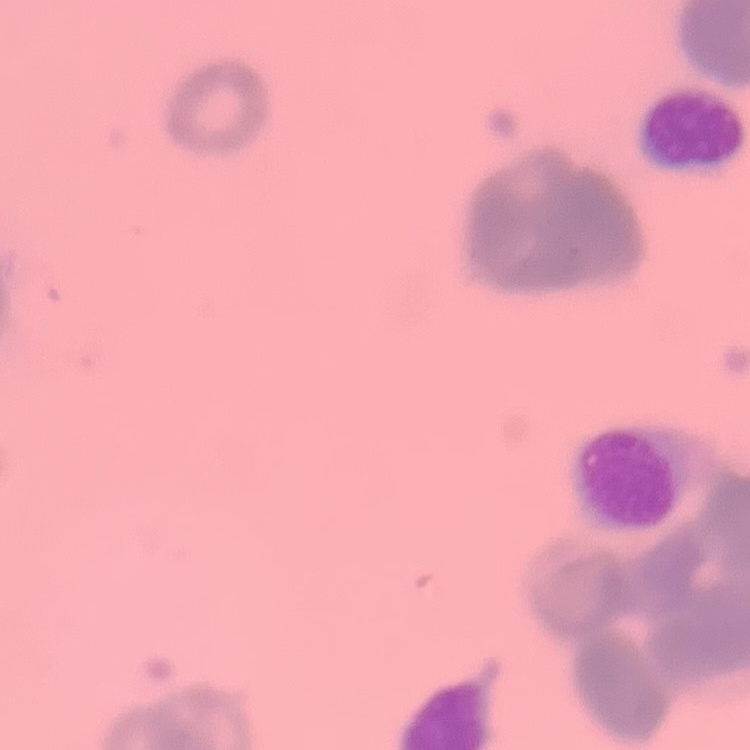

erythrocyte morphology = rouleaux formation
image type = square crop of a larger photomicrograph
preparation = thin blood smear
stain = Field's or Giemsa